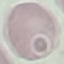
Summary:
  - Result: no malaria parasites seen
  - Stain: Giemsa
  - Capture: smartphone camera at the microscope eyepiece
  - Image type: automatically extracted cell patch, resized to 64 × 64 pixels
  - Preparation: thin smear